Report the malaria status of this cell.
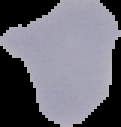

It is uninfected.

preparation = thin blood film
image type = cell region segmented out of the field of view; surrounding area masked to black
image size = 121×127 pixels